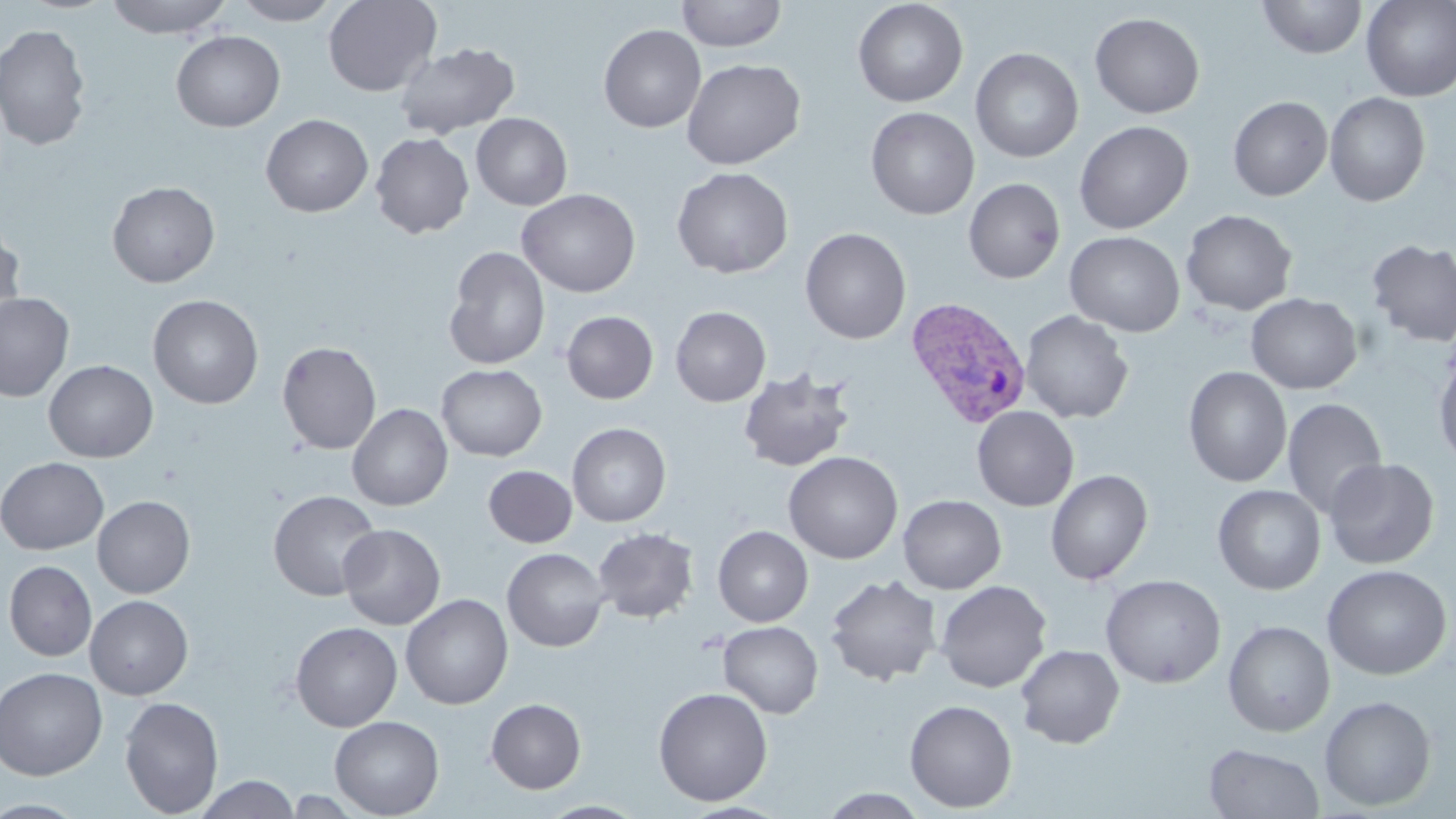

Approximate bounding boxes as named x1/y1/x2/y2 corners in pixels. Uninfected red blood cell locations: (x1=105, y1=0, x2=234, y2=38), (x1=232, y1=0, x2=342, y2=25), (x1=323, y1=0, x2=440, y2=96), (x1=675, y1=0, x2=788, y2=52), (x1=852, y1=0, x2=968, y2=107), (x1=1257, y1=0, x2=1367, y2=59), (x1=1360, y1=0, x2=1456, y2=102), (x1=1090, y1=12, x2=1205, y2=118), (x1=0, y1=22, x2=92, y2=151), (x1=598, y1=24, x2=706, y2=133), (x1=171, y1=31, x2=285, y2=132), (x1=394, y1=42, x2=520, y2=139), (x1=970, y1=47, x2=1083, y2=163), (x1=682, y1=58, x2=806, y2=170), (x1=1325, y1=92, x2=1430, y2=207), (x1=1227, y1=96, x2=1333, y2=201), (x1=865, y1=107, x2=979, y2=219), (x1=471, y1=113, x2=572, y2=210), (x1=261, y1=114, x2=373, y2=217), (x1=1074, y1=120, x2=1193, y2=234), (x1=370, y1=132, x2=474, y2=238), (x1=671, y1=166, x2=793, y2=278), (x1=963, y1=178, x2=1066, y2=283), (x1=107, y1=181, x2=220, y2=287), (x1=517, y1=189, x2=640, y2=297), (x1=1181, y1=209, x2=1298, y2=315), (x1=0, y1=224, x2=25, y2=334), (x1=799, y1=227, x2=911, y2=344), (x1=1065, y1=231, x2=1185, y2=337), (x1=1366, y1=239, x2=1456, y2=347), (x1=443, y1=246, x2=550, y2=369), (x1=1, y1=292, x2=74, y2=402), (x1=1246, y1=293, x2=1362, y2=394), (x1=148, y1=294, x2=263, y2=409), (x1=670, y1=306, x2=771, y2=406), (x1=1020, y1=310, x2=1134, y2=423), (x1=562, y1=311, x2=658, y2=404), (x1=277, y1=341, x2=382, y2=454), (x1=1434, y1=353, x2=1456, y2=470), (x1=44, y1=360, x2=157, y2=462), (x1=436, y1=364, x2=547, y2=461), (x1=737, y1=365, x2=855, y2=472), (x1=1183, y1=366, x2=1292, y2=487), (x1=1281, y1=398, x2=1388, y2=518), (x1=347, y1=403, x2=452, y2=511), (x1=972, y1=406, x2=1079, y2=512), (x1=567, y1=422, x2=671, y2=526), (x1=783, y1=451, x2=903, y2=564), (x1=0, y1=457, x2=108, y2=555), (x1=1323, y1=457, x2=1440, y2=570), (x1=484, y1=465, x2=577, y2=547), (x1=1045, y1=469, x2=1153, y2=585), (x1=1212, y1=484, x2=1326, y2=595), (x1=268, y1=490, x2=382, y2=601), (x1=897, y1=494, x2=1006, y2=594), (x1=92, y1=495, x2=195, y2=598), (x1=338, y1=523, x2=445, y2=630), (x1=712, y1=525, x2=813, y2=627), (x1=593, y1=527, x2=698, y2=623), (x1=502, y1=547, x2=609, y2=651), (x1=4, y1=560, x2=97, y2=661), (x1=1321, y1=564, x2=1452, y2=680), (x1=1101, y1=574, x2=1226, y2=688), (x1=824, y1=575, x2=944, y2=686), (x1=935, y1=580, x2=1053, y2=693), (x1=401, y1=593, x2=513, y2=710), (x1=85, y1=595, x2=194, y2=699), (x1=1222, y1=620, x2=1336, y2=737), (x1=718, y1=621, x2=823, y2=718), (x1=290, y1=622, x2=402, y2=732), (x1=1016, y1=644, x2=1124, y2=749), (x1=0, y1=666, x2=107, y2=780), (x1=653, y1=687, x2=773, y2=806), (x1=1319, y1=695, x2=1437, y2=811), (x1=119, y1=696, x2=223, y2=817), (x1=485, y1=698, x2=586, y2=794), (x1=905, y1=699, x2=1017, y2=813), (x1=329, y1=716, x2=444, y2=819), (x1=1203, y1=744, x2=1324, y2=819), (x1=195, y1=775, x2=300, y2=818), (x1=818, y1=788, x2=931, y2=818), (x1=285, y1=789, x2=366, y2=817), (x1=0, y1=798, x2=90, y2=818), (x1=537, y1=800, x2=648, y2=818). Plasmodium vivax-infected red blood cell locations: (x1=905, y1=297, x2=1031, y2=430). Slide-level diagnosis: Plasmodium vivax. May-Grünwald-Giemsa stain. Thin blood film. 1000x magnification. Image is 1456×819 pixels. Optical microscopy. Single field of view.